State which parasite is depicted.
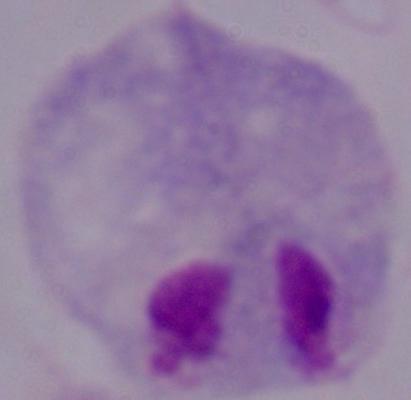
This is a trichomonad.

{
  "magnification": "1000x",
  "modality": "micrograph"
}